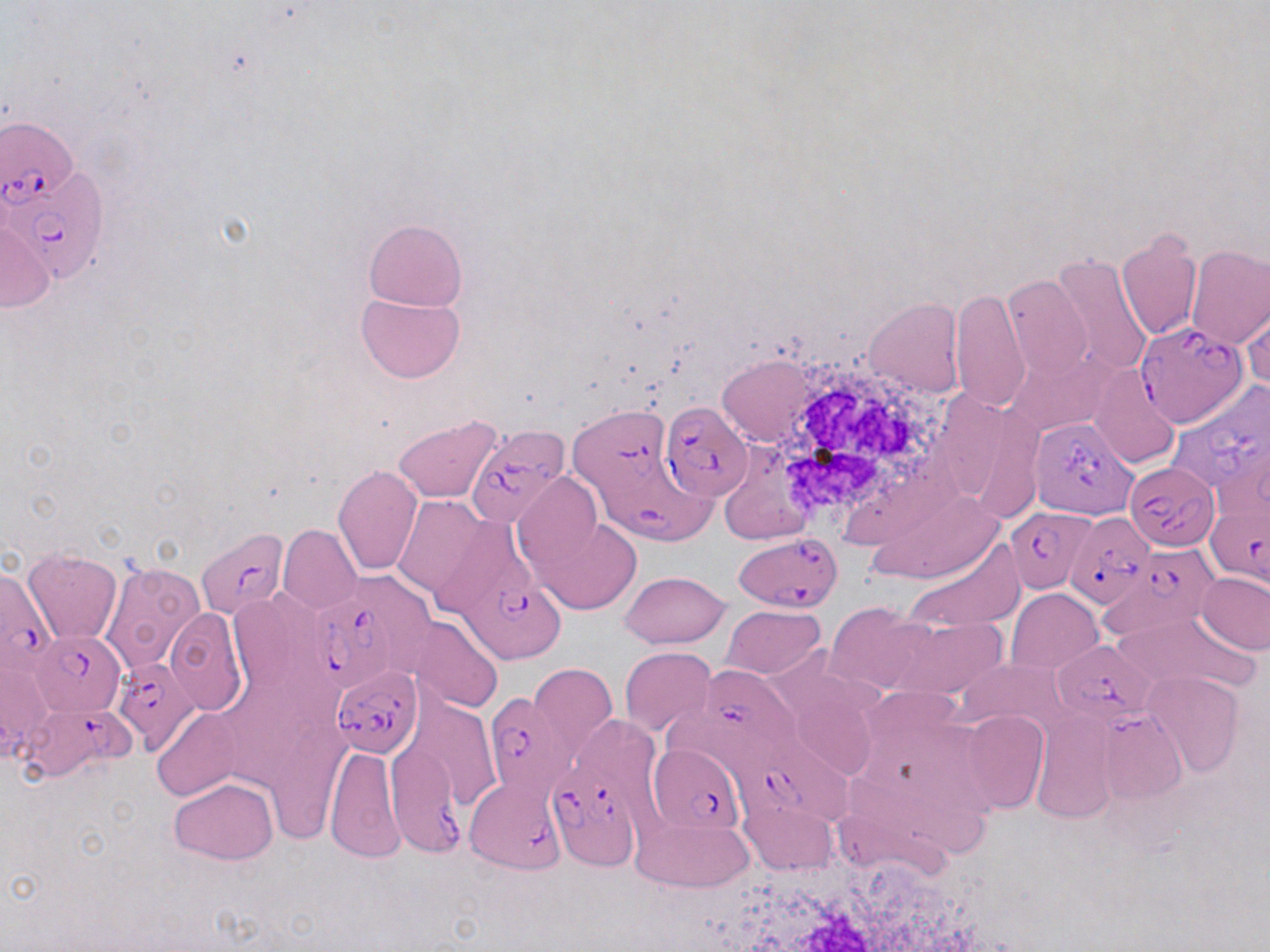
slide-level diagnosis = Plasmodium falciparum
field of view = single
modality = optical microscopy
white blood cell locations = approximate bounding boxes as (x1,y1)-(x2,y2) corner pairs in pixels: (765,355)-(949,522), (720,847)-(994,952)
preparation = thin blood smear
uninfected red blood cell locations = approximate bounding boxes as (x1,y1)-(x2,y2) corner pairs in pixels: (363,218)-(467,311), (0,220)-(54,313), (1116,228)-(1203,341), (1185,243)-(1269,350), (1050,254)-(1154,382), (1001,272)-(1092,380), (950,287)-(1029,414), (355,292)-(464,384), (863,299)-(964,397), (1242,301)-(1270,390), (716,353)-(824,447), (1088,365)-(1181,467), (392,417)-(502,502), (333,464)-(423,576), (512,473)-(609,579), (860,488)-(1006,585), (393,495)-(492,601), (536,515)-(641,612), (278,525)-(361,613), (907,537)-(1025,634), (23,549)-(122,642), (99,561)-(206,676), (620,570)-(731,647), (1197,570)-(1270,655), (1007,588)-(1104,674), (720,604)-(826,678), (826,604)-(933,696), (164,607)-(246,715), (1111,612)-(1256,694), (407,616)-(504,714), (888,616)-(1006,700), (620,647)-(716,737), (1,657)-(50,760), (958,660)-(1066,732), (529,662)-(618,764), (1143,672)-(1244,777), (403,694)-(501,812), (153,708)-(241,801), (960,709)-(1049,815), (1031,711)-(1117,824), (324,743)-(405,863), (170,778)-(278,864), (739,799)-(837,876), (631,813)-(752,893)
stain = May-Grünwald-Giemsa
magnification = 1000x
Plasmodium falciparum-infected red blood cell locations = approximate bounding boxes as (x1,y1)-(x2,y2) corner pairs in pixels: (1,117)-(84,236), (6,162)-(108,286), (1135,316)-(1245,428), (1166,380)-(1267,503), (659,401)-(754,500), (570,408)-(674,499), (1029,416)-(1137,519), (466,424)-(569,525), (1126,458)-(1221,549), (598,469)-(721,547), (1204,502)-(1270,589), (1005,506)-(1096,592), (1065,511)-(1155,609), (197,529)-(287,621), (734,532)-(843,611), (1093,549)-(1227,641), (0,568)-(57,680), (464,572)-(566,663), (306,596)-(398,695), (30,633)-(124,717), (1052,637)-(1160,724), (113,655)-(202,753), (701,664)-(801,763), (330,665)-(423,756), (485,694)-(576,801), (22,701)-(132,778), (1099,709)-(1186,803), (384,736)-(461,856), (725,742)-(855,825), (648,744)-(749,833), (549,758)-(639,873), (464,777)-(566,873)
image size = 1270×952 pixels